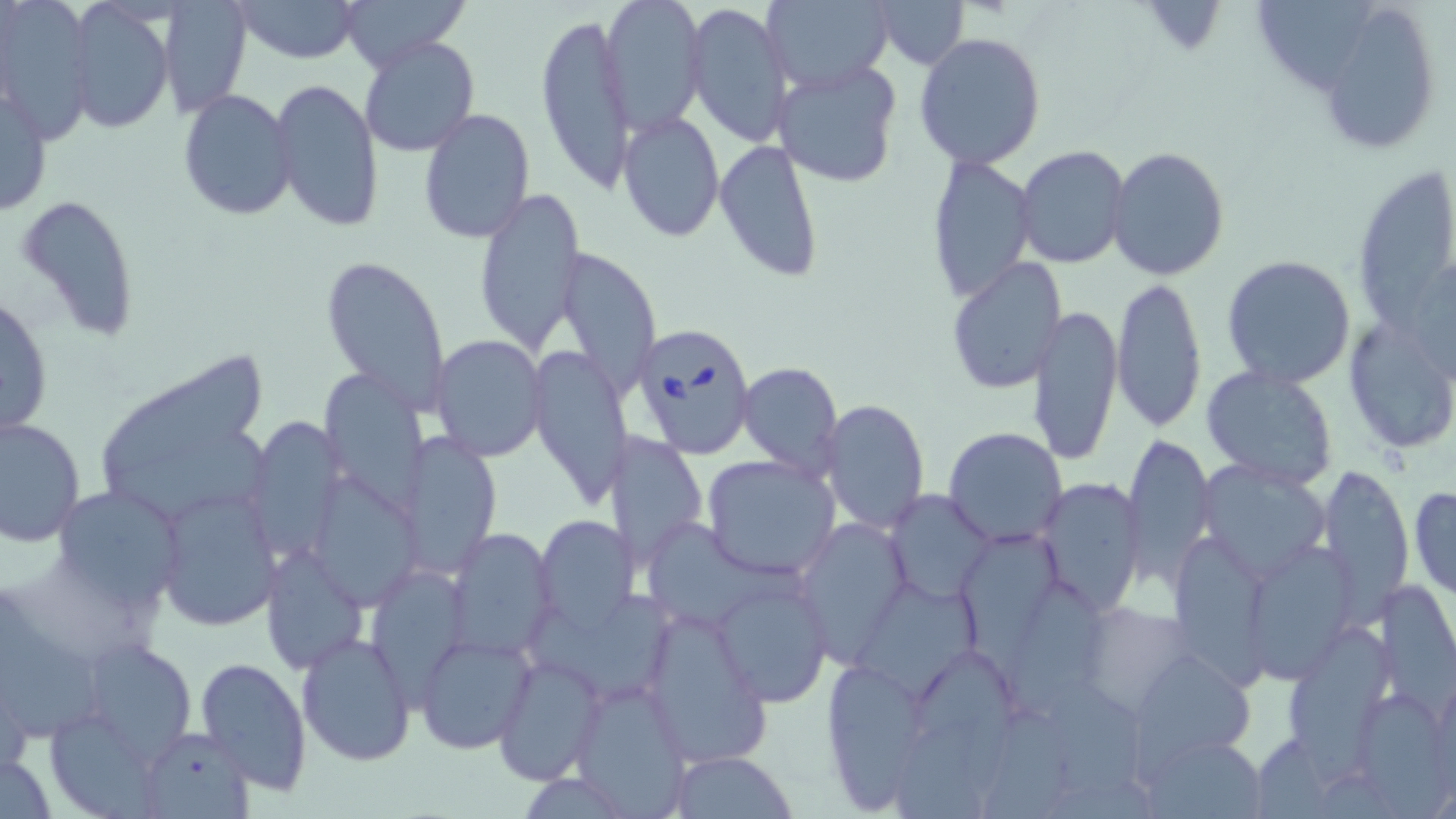 Approximate bounding boxes as named x1/y1/x2/y2 corners in pixels. Uninfected red blood cell locations: (x1=154, y1=0, x2=250, y2=113), (x1=232, y1=0, x2=362, y2=63), (x1=338, y1=0, x2=472, y2=69), (x1=597, y1=0, x2=705, y2=134), (x1=761, y1=0, x2=896, y2=93), (x1=872, y1=0, x2=969, y2=68), (x1=1254, y1=0, x2=1376, y2=93), (x1=685, y1=2, x2=792, y2=149), (x1=1311, y1=2, x2=1444, y2=152), (x1=63, y1=3, x2=174, y2=131), (x1=0, y1=4, x2=94, y2=141), (x1=535, y1=8, x2=636, y2=196), (x1=357, y1=32, x2=482, y2=158), (x1=914, y1=32, x2=1046, y2=170), (x1=772, y1=60, x2=903, y2=189), (x1=268, y1=77, x2=383, y2=232), (x1=1, y1=81, x2=51, y2=219), (x1=177, y1=89, x2=298, y2=220), (x1=419, y1=106, x2=535, y2=243), (x1=618, y1=109, x2=725, y2=242), (x1=715, y1=137, x2=825, y2=282), (x1=1016, y1=144, x2=1131, y2=268), (x1=1106, y1=147, x2=1230, y2=283), (x1=926, y1=153, x2=1037, y2=305), (x1=1352, y1=164, x2=1456, y2=329), (x1=473, y1=186, x2=587, y2=356), (x1=16, y1=196, x2=142, y2=344), (x1=553, y1=244, x2=662, y2=397), (x1=320, y1=253, x2=453, y2=416), (x1=1222, y1=254, x2=1357, y2=388), (x1=947, y1=257, x2=1070, y2=394), (x1=1111, y1=277, x2=1207, y2=433), (x1=1, y1=290, x2=55, y2=441), (x1=1027, y1=304, x2=1122, y2=466), (x1=1343, y1=313, x2=1453, y2=456), (x1=429, y1=334, x2=549, y2=462), (x1=526, y1=346, x2=634, y2=508), (x1=100, y1=352, x2=267, y2=479), (x1=736, y1=359, x2=844, y2=479), (x1=1201, y1=366, x2=1340, y2=491), (x1=322, y1=371, x2=431, y2=518), (x1=820, y1=397, x2=931, y2=535), (x1=0, y1=414, x2=85, y2=546), (x1=244, y1=417, x2=344, y2=560), (x1=943, y1=426, x2=1068, y2=546), (x1=604, y1=429, x2=708, y2=570), (x1=103, y1=431, x2=279, y2=519), (x1=1124, y1=432, x2=1216, y2=586), (x1=400, y1=434, x2=501, y2=575), (x1=701, y1=454, x2=840, y2=579), (x1=1198, y1=459, x2=1333, y2=580), (x1=1318, y1=465, x2=1413, y2=611), (x1=314, y1=475, x2=425, y2=612), (x1=1035, y1=476, x2=1146, y2=618), (x1=50, y1=486, x2=188, y2=609), (x1=1409, y1=486, x2=1456, y2=598), (x1=884, y1=489, x2=995, y2=600), (x1=156, y1=490, x2=278, y2=631), (x1=534, y1=515, x2=640, y2=638), (x1=795, y1=518, x2=913, y2=663), (x1=956, y1=523, x2=1060, y2=683), (x1=645, y1=528, x2=804, y2=627), (x1=448, y1=529, x2=556, y2=661), (x1=1175, y1=535, x2=1266, y2=689), (x1=262, y1=545, x2=368, y2=675), (x1=1251, y1=546, x2=1355, y2=682), (x1=370, y1=568, x2=466, y2=723), (x1=711, y1=571, x2=834, y2=707), (x1=1005, y1=579, x2=1103, y2=720), (x1=1377, y1=579, x2=1456, y2=698), (x1=859, y1=586, x2=983, y2=703), (x1=529, y1=591, x2=677, y2=702), (x1=0, y1=597, x2=109, y2=747), (x1=642, y1=603, x2=777, y2=756), (x1=1075, y1=603, x2=1194, y2=716), (x1=1289, y1=623, x2=1394, y2=791), (x1=298, y1=631, x2=417, y2=765), (x1=417, y1=634, x2=534, y2=754), (x1=73, y1=637, x2=198, y2=767), (x1=917, y1=647, x2=1012, y2=798), (x1=1130, y1=653, x2=1247, y2=783), (x1=492, y1=654, x2=606, y2=784), (x1=820, y1=654, x2=932, y2=809), (x1=195, y1=656, x2=311, y2=798), (x1=571, y1=679, x2=690, y2=815), (x1=1050, y1=682, x2=1149, y2=799), (x1=1361, y1=691, x2=1452, y2=818), (x1=983, y1=707, x2=1076, y2=819), (x1=53, y1=716, x2=167, y2=819), (x1=896, y1=717, x2=986, y2=819), (x1=135, y1=727, x2=257, y2=818), (x1=1147, y1=735, x2=1267, y2=816), (x1=667, y1=750, x2=797, y2=818), (x1=1, y1=751, x2=58, y2=818). Babesia divergens-infected red blood cell locations: (x1=631, y1=321, x2=759, y2=459). Slide-level diagnosis: Babesia divergens. May-Grünwald-Giemsa stain. Captured at 1000x magnification. Optical microscopy. Thin blood smear. Image is 1456×819 pixels. One field of a larger specimen.